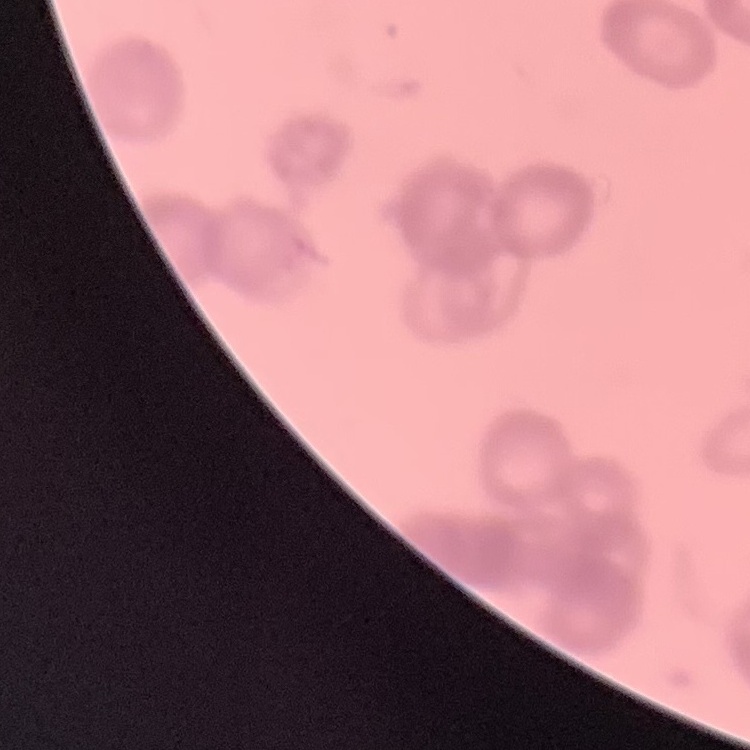
Summary:
  - Erythrocyte morphology: rouleaux formation
  - Preparation: thin blood smear
  - Image type: square crop of a larger photomicrograph
  - Stain: Field's or Giemsa